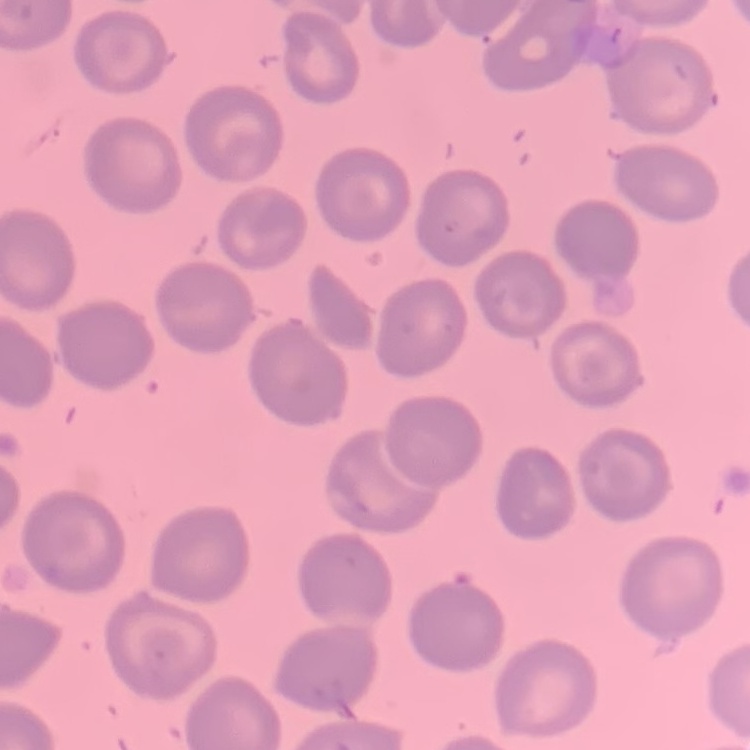
Summary:
  - Erythrocyte morphology: no rouleaux formation
  - Preparation: thin peripheral smear
  - Image type: square crop of a larger photomicrograph
  - Stain: Field's or Giemsa